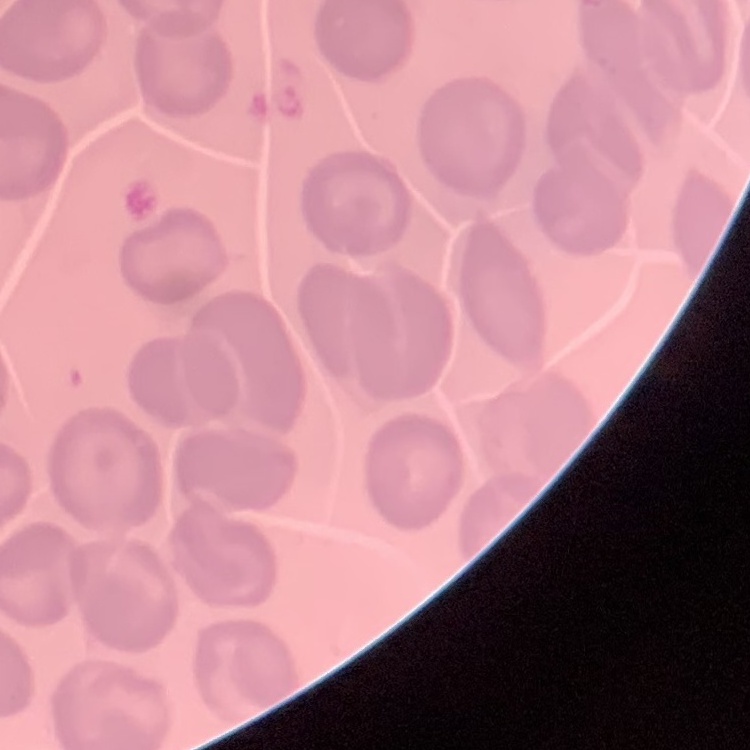
Summary:
  - Erythrocyte morphology: no rouleaux formation
  - Image type: square crop of a larger photomicrograph
  - Stain: Field's or Giemsa
  - Preparation: thin blood film